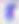

identification = Toxoplasma gondii
modality = micrograph
magnification = 400x